Locate every blood parasite and identify its species.
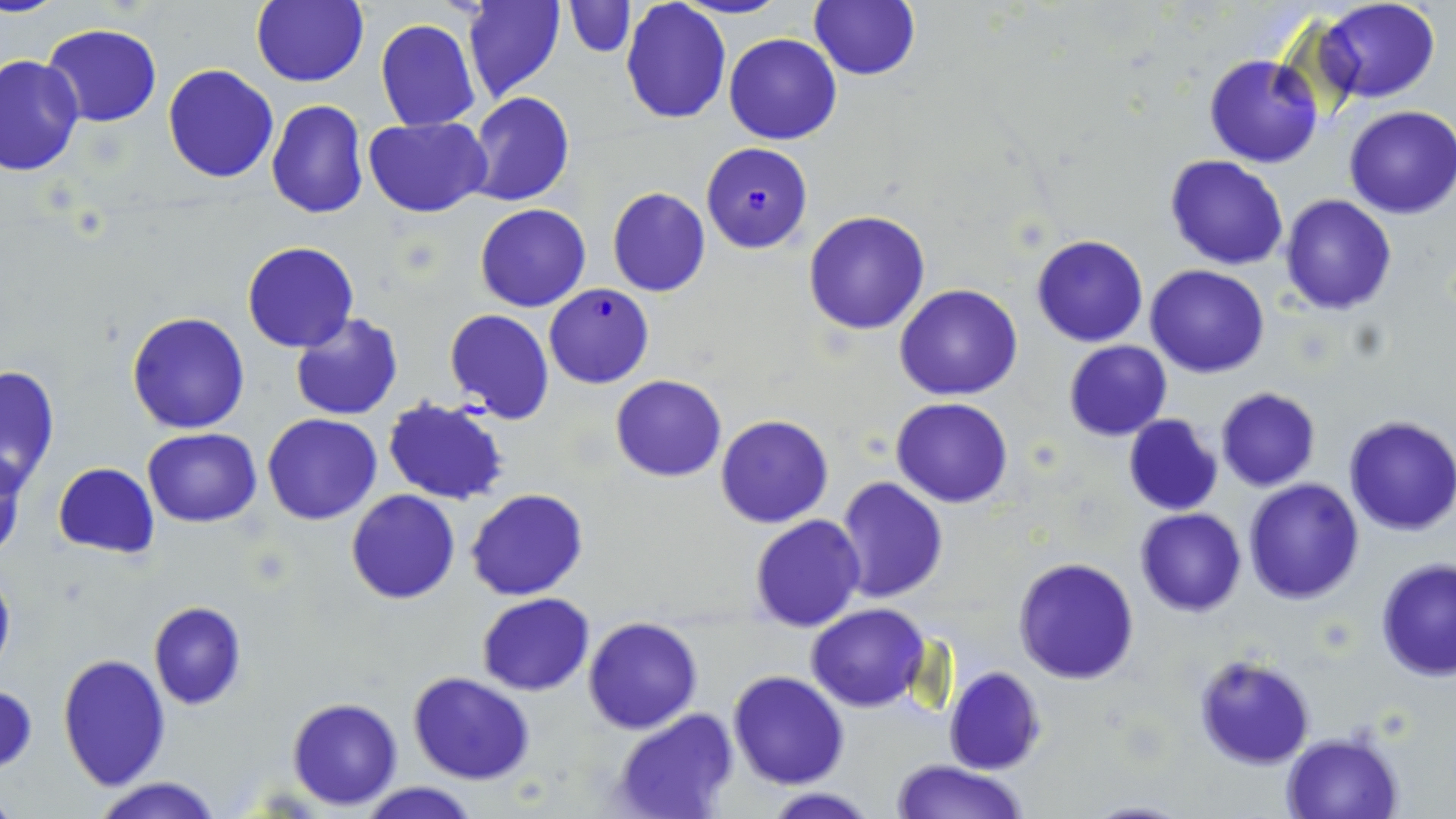

Approximate bounding boxes as named x1/y1/x2/y2 corners in pixels.
Plasmodium falciparum-infected red blood cells: (x1=701, y1=143, x2=813, y2=252), (x1=543, y1=284, x2=655, y2=388).
No Plasmodium ovale, Plasmodium malariae, Plasmodium vivax, Babesia divergens, or Trypanosoma brucei observed.

Uninfected red blood cell locations: (x1=250, y1=0, x2=369, y2=88), (x1=462, y1=0, x2=566, y2=103), (x1=620, y1=0, x2=732, y2=125), (x1=676, y1=0, x2=789, y2=20), (x1=809, y1=0, x2=920, y2=82), (x1=1315, y1=0, x2=1439, y2=103), (x1=563, y1=1, x2=635, y2=57), (x1=374, y1=18, x2=481, y2=131), (x1=43, y1=25, x2=161, y2=127), (x1=724, y1=32, x2=842, y2=144), (x1=0, y1=53, x2=84, y2=176), (x1=1204, y1=54, x2=1322, y2=168), (x1=163, y1=64, x2=279, y2=182), (x1=465, y1=91, x2=574, y2=206), (x1=266, y1=100, x2=368, y2=219), (x1=1344, y1=105, x2=1456, y2=219), (x1=364, y1=117, x2=492, y2=216), (x1=1164, y1=155, x2=1290, y2=271), (x1=607, y1=187, x2=711, y2=296), (x1=1279, y1=195, x2=1396, y2=315), (x1=474, y1=203, x2=591, y2=312), (x1=803, y1=209, x2=932, y2=335), (x1=1030, y1=235, x2=1148, y2=347), (x1=242, y1=241, x2=358, y2=352), (x1=1146, y1=265, x2=1269, y2=378), (x1=895, y1=284, x2=1022, y2=401), (x1=443, y1=308, x2=554, y2=424), (x1=126, y1=311, x2=250, y2=435), (x1=289, y1=312, x2=404, y2=421), (x1=1064, y1=340, x2=1172, y2=441), (x1=0, y1=364, x2=61, y2=490), (x1=610, y1=374, x2=727, y2=481), (x1=1215, y1=388, x2=1321, y2=491), (x1=891, y1=396, x2=1014, y2=508), (x1=383, y1=397, x2=510, y2=506), (x1=263, y1=414, x2=383, y2=524), (x1=716, y1=414, x2=833, y2=528), (x1=1122, y1=416, x2=1223, y2=516), (x1=1342, y1=416, x2=1456, y2=536), (x1=142, y1=428, x2=263, y2=527), (x1=0, y1=449, x2=29, y2=561), (x1=52, y1=463, x2=159, y2=560), (x1=834, y1=476, x2=949, y2=604), (x1=1244, y1=479, x2=1364, y2=603), (x1=466, y1=489, x2=589, y2=602), (x1=346, y1=490, x2=460, y2=605), (x1=1135, y1=508, x2=1246, y2=616), (x1=749, y1=514, x2=866, y2=631), (x1=1013, y1=556, x2=1141, y2=684), (x1=1376, y1=559, x2=1456, y2=681), (x1=0, y1=563, x2=16, y2=679), (x1=476, y1=593, x2=594, y2=696), (x1=148, y1=601, x2=247, y2=710), (x1=806, y1=603, x2=929, y2=713), (x1=582, y1=616, x2=703, y2=734), (x1=57, y1=651, x2=171, y2=791), (x1=1193, y1=654, x2=1315, y2=769), (x1=943, y1=666, x2=1045, y2=775), (x1=727, y1=670, x2=850, y2=789), (x1=407, y1=672, x2=536, y2=786), (x1=287, y1=697, x2=403, y2=810), (x1=609, y1=710, x2=738, y2=819), (x1=1281, y1=732, x2=1403, y2=819), (x1=890, y1=760, x2=1030, y2=818), (x1=93, y1=777, x2=223, y2=819), (x1=357, y1=782, x2=483, y2=818), (x1=761, y1=786, x2=878, y2=818). Slide-level diagnosis: Plasmodium falciparum. Single field of view. 1000x magnification. Image is 1456×819 pixels. Thin blood film. May-Grünwald-Giemsa stain. Optical microscopy.